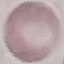
Summary:
  - Malaria status: uninfected
  - Stain: Giemsa
  - Image type: automatically extracted cell patch, resized to 64 × 64 pixels
  - Preparation: thin blood smear
  - Capture: smartphone through the microscope eyepiece